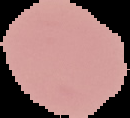

Image is 130×118 pixels. Malaria status: uninfected. From a thin blood smear. Cell region segmented out of the field of view; the surrounding area is masked to black.